Comment on the morphology of the red blood cells.
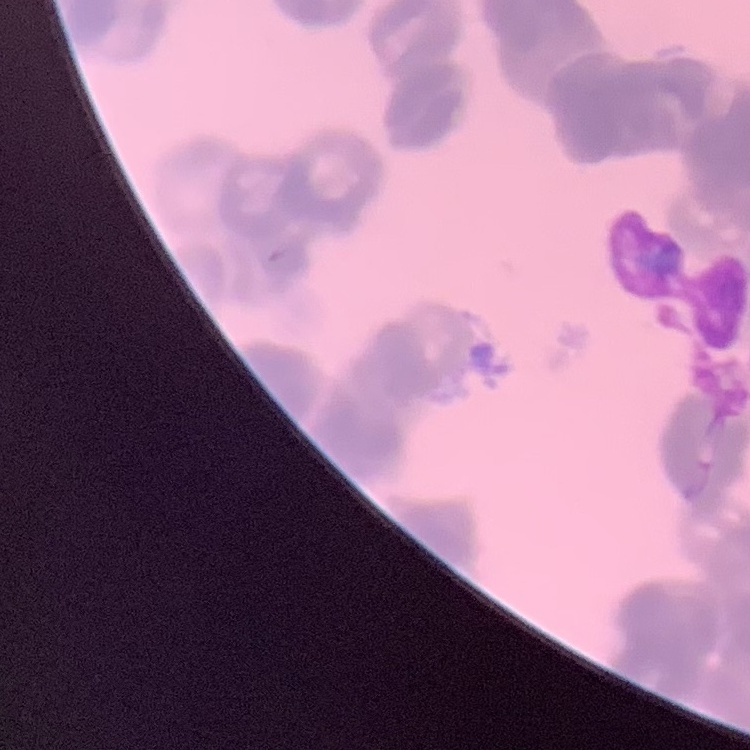

They show rouleaux formation.

Summary:
  - Preparation: thin blood smear
  - Image type: one tile cut from a larger photomicrograph
  - Stain: Field's or Giemsa